Classify this cell by malaria status.
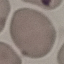
It is uninfected.

{
  "capture": "smartphone through the microscope eyepiece",
  "preparation": "thin blood film",
  "stain": "Giemsa",
  "image_type": "cell patch, automatically extracted from a larger field of view and resized to 64 × 64 pixels"
}